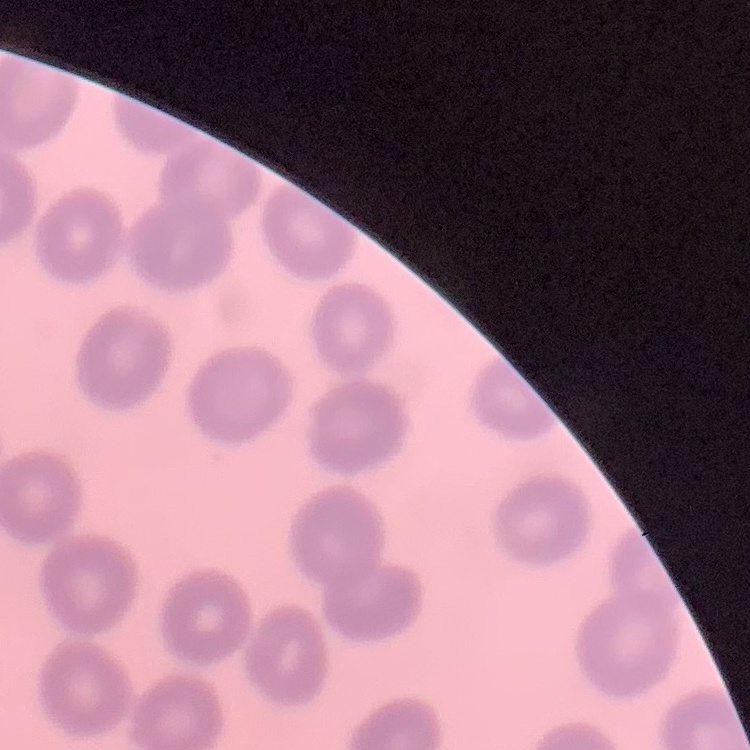

erythrocyte_morphology: no rouleaux formation
stain: Field's or Giemsa
preparation: thin blood smear
image_type: one tile cut from a larger photomicrograph